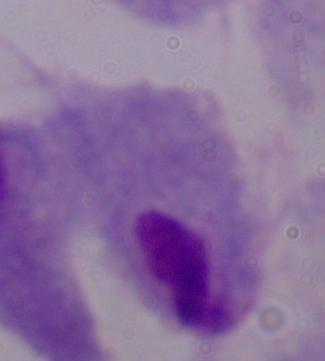
Summary:
  - Identification: trichomonad
  - Magnification: 1000x
  - Modality: photomicrograph